Identify the blood parasite species.
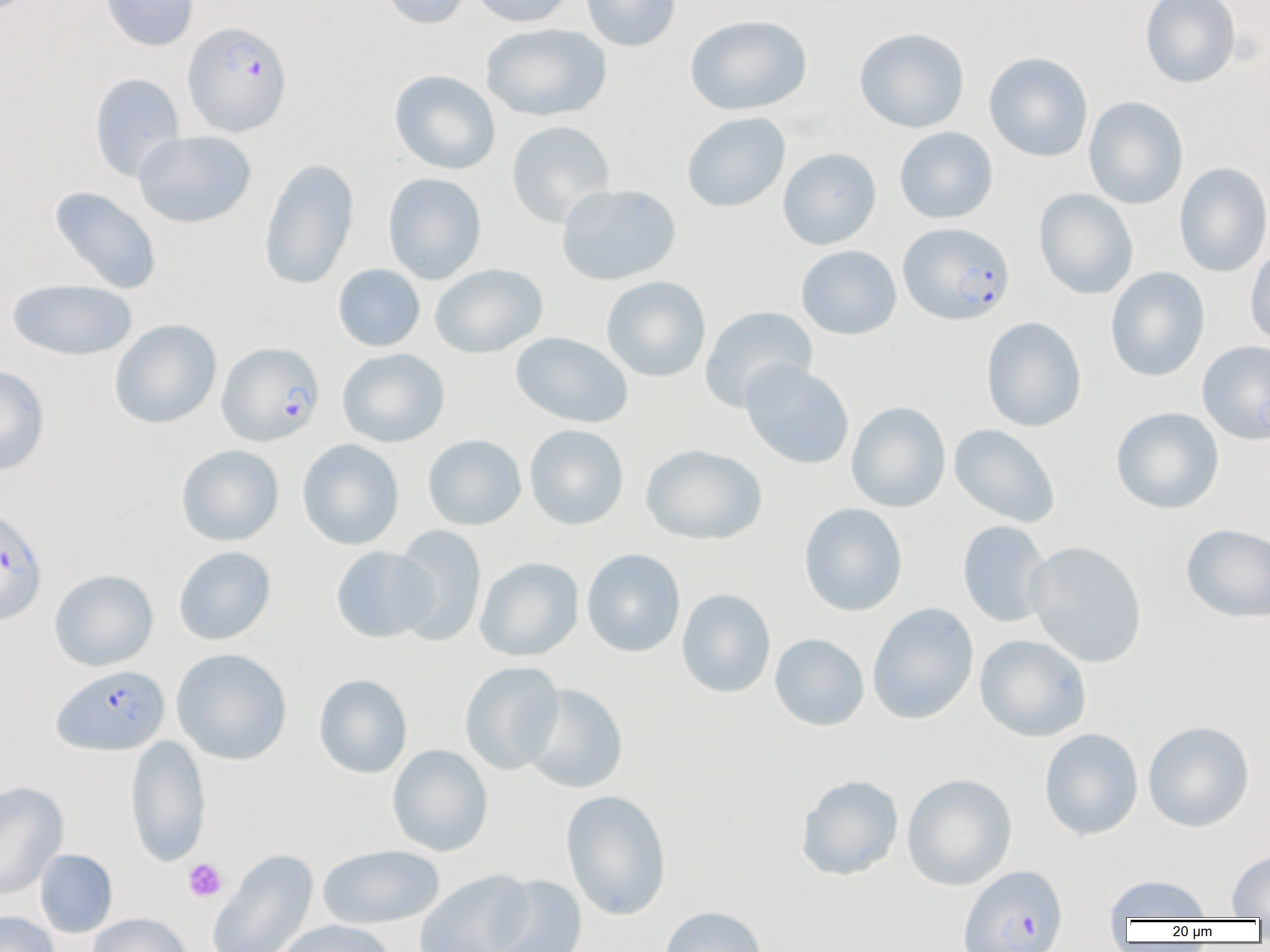

Plasmodium falciparum.

magnification = 1000x
uninfected red blood cell locations = approximate bounding boxes as [x1, y1, x2, y2] in pixels: [99, 0, 198, 51], [379, 0, 472, 29], [469, 0, 576, 27], [580, 0, 681, 52], [1139, 0, 1241, 89], [685, 14, 811, 115], [480, 23, 612, 122], [854, 28, 970, 132], [984, 52, 1093, 162], [389, 69, 501, 175], [88, 72, 186, 182], [1083, 96, 1188, 209], [681, 111, 791, 213], [506, 120, 615, 228], [894, 126, 998, 224], [133, 130, 256, 228], [777, 147, 882, 250], [258, 157, 360, 291], [1173, 162, 1270, 277], [383, 172, 487, 284], [556, 183, 681, 286], [49, 186, 162, 294], [1034, 188, 1138, 299], [1245, 241, 1270, 349], [796, 245, 902, 340], [333, 264, 425, 352], [430, 264, 548, 358], [1106, 267, 1210, 381], [601, 276, 711, 383], [7, 279, 137, 361], [699, 306, 818, 412], [981, 317, 1087, 432], [109, 319, 222, 429], [510, 332, 633, 428], [1197, 340, 1270, 445], [337, 348, 450, 448], [739, 359, 854, 470], [0, 366, 50, 476], [846, 401, 951, 512], [1111, 407, 1224, 514], [524, 424, 629, 530], [949, 424, 1060, 527], [422, 434, 527, 530], [297, 439, 404, 550], [176, 444, 284, 545], [640, 444, 767, 545], [798, 503, 908, 616], [957, 520, 1052, 627], [1181, 524, 1269, 622], [390, 525, 487, 646], [1025, 541, 1147, 667], [173, 546, 276, 645], [330, 546, 439, 643], [582, 548, 686, 657], [472, 557, 574, 774], [474, 557, 584, 661], [49, 569, 158, 671], [676, 588, 775, 698], [867, 602, 979, 725], [769, 633, 869, 731], [975, 634, 1092, 741], [171, 648, 292, 765], [460, 661, 564, 775], [313, 673, 412, 778], [521, 684, 628, 793], [1142, 720, 1255, 832], [1039, 727, 1143, 841], [125, 734, 211, 867], [387, 744, 493, 856], [795, 774, 904, 881], [902, 774, 1017, 891], [0, 781, 69, 899], [560, 789, 672, 921], [317, 844, 445, 929], [34, 848, 118, 938], [208, 848, 318, 951], [1227, 850, 1270, 918], [415, 869, 535, 952], [1102, 874, 1214, 921], [486, 875, 588, 952], [659, 905, 768, 952], [0, 910, 59, 952], [87, 912, 192, 952], [273, 920, 397, 952]
field of view = one of a larger specimen
platelet locations = approximate bounding boxes as [x1, y1, x2, y2] in pixels: [183, 858, 227, 902]
preparation = thin blood smear
Plasmodium falciparum-infected red blood cell locations = approximate bounding boxes as [x1, y1, x2, y2] in pixels: [182, 21, 293, 136], [898, 222, 1015, 326], [217, 342, 325, 446], [0, 506, 48, 626], [51, 665, 169, 756], [958, 864, 1069, 952]
modality = optical microscopy
image size = 1270×952 pixels